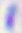
identification = Toxoplasma gondii
magnification = 400x
modality = micrograph